Locate every Plasmodium parasite.
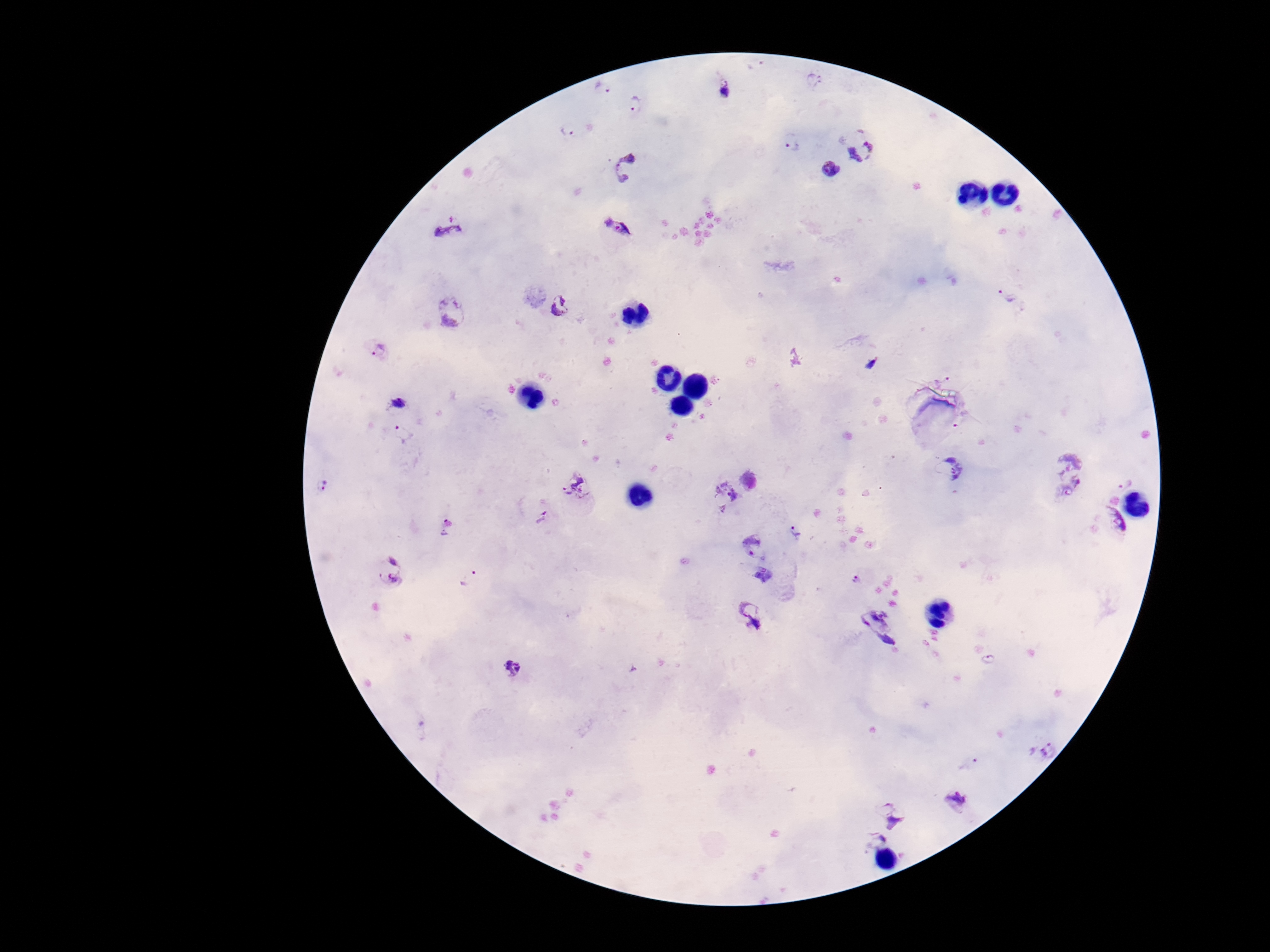

Approximate object centers, in pixels from the top-left corner.
Plasmodium parasites: (x=757, y=68), (x=812, y=82), (x=604, y=91), (x=726, y=91), (x=638, y=108), (x=568, y=129), (x=792, y=143), (x=864, y=149), (x=626, y=165), (x=829, y=171), (x=448, y=227), (x=621, y=227), (x=1005, y=297), (x=562, y=308), (x=453, y=315), (x=377, y=349), (x=872, y=363), (x=943, y=377), (x=399, y=403), (x=402, y=435), (x=949, y=469), (x=1071, y=473), (x=1126, y=476), (x=322, y=485), (x=582, y=485), (x=720, y=494), (x=541, y=519), (x=448, y=526), (x=1101, y=529), (x=797, y=535), (x=754, y=543), (x=390, y=569), (x=767, y=576), (x=469, y=578), (x=858, y=579), (x=750, y=616), (x=879, y=625), (x=988, y=658), (x=512, y=670), (x=420, y=728), (x=1041, y=751), (x=970, y=764), (x=954, y=803), (x=892, y=808), (x=873, y=839).

Single field of view. Giemsa stain. Patient malaria status: positive. Thick blood smear. 100x magnification. Smartphone photograph taken through the microscope eyepiece. Image is 1270×952 pixels.